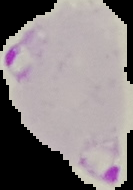

Summary:
  - Image size: 133×190 pixels
  - Preparation: thin blood film
  - Result: malaria parasites identified
  - Image type: cell region segmented out of the field of view; surrounding area masked to black